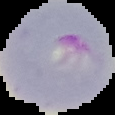

malaria status = parasitized
preparation = thin blood smear
image size = 115×115 pixels
image type = segmented cell region with the area outside set to black